State which parasite is depicted.
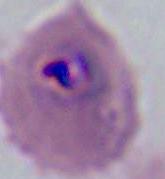

This is Plasmodium.

Micrograph. 400x or 1000x magnification.